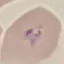 Malaria status: uninfected. Giemsa-stained preparation. Photographed with a smartphone camera at the microscope eyepiece. Cell patch, automatically extracted from a larger field of view and resized to 64 × 64 pixels. Thin blood smear.